State which parasite is depicted.
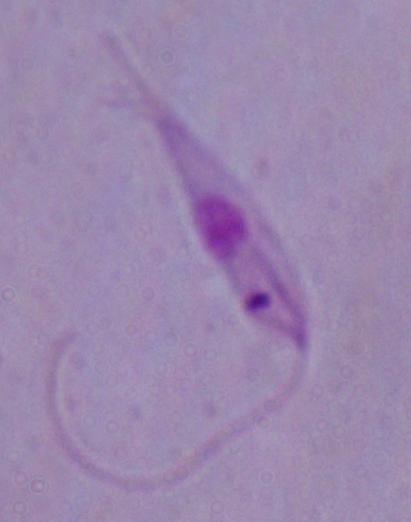
This is Leishmania.

Micrograph. Captured at 1000x magnification.